Report the malaria status of this cell.
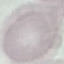

Uninfected.

Giemsa stain. Photographed with a smartphone camera at the microscope eyepiece. Automatically extracted cell patch, resized to 64 × 64 pixels. Thin blood smear.